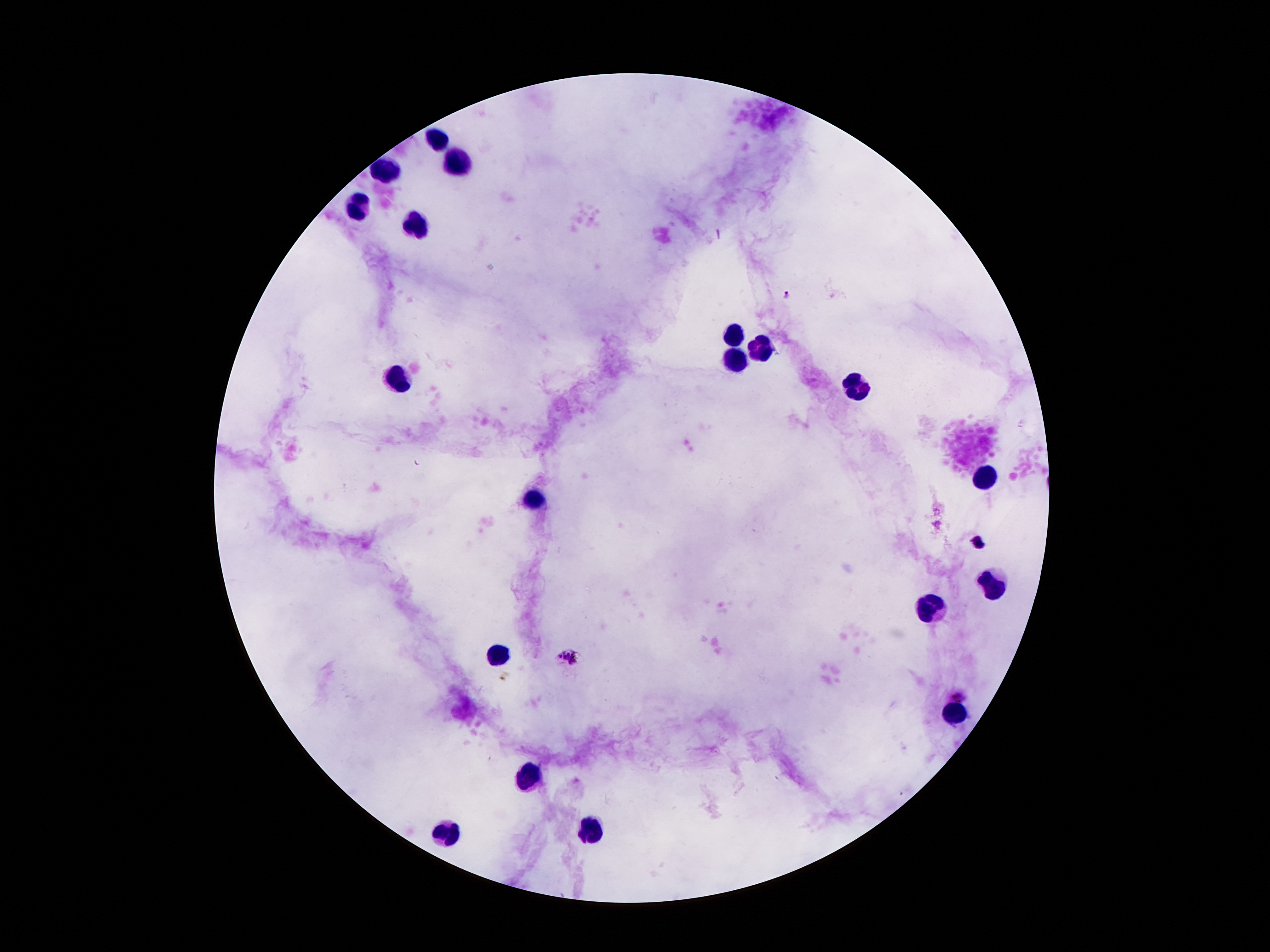
Approximate centers as {x, y} in pixels. Leukocyte locations: {442, 137}, {460, 162}, {388, 173}, {360, 204}, {415, 224}, {735, 332}, {763, 348}, {735, 359}, {399, 381}, {859, 387}, {985, 480}, {537, 497}, {994, 585}, {931, 609}, {502, 656}, {948, 714}, {528, 774}, {594, 827}, {444, 831}. Plasmodium parasite locations: {787, 295}, {569, 659}, {959, 694}. Photographed through the microscope eyepiece with a smartphone camera. Giemsa stain. 100x magnification. Patient malaria status: positive for Plasmodium falciparum. Thick peripheral-blood smear. Image is 1270×952 pixels. Single field of view.